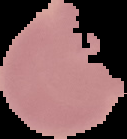
Summary:
  - Image size: 127×139 pixels
  - Preparation: thin blood film
  - Result: no malaria parasites detected
  - Image type: cell region segmented out of the field of view; surrounding area masked to black